Outline each uninfected red blood cell.
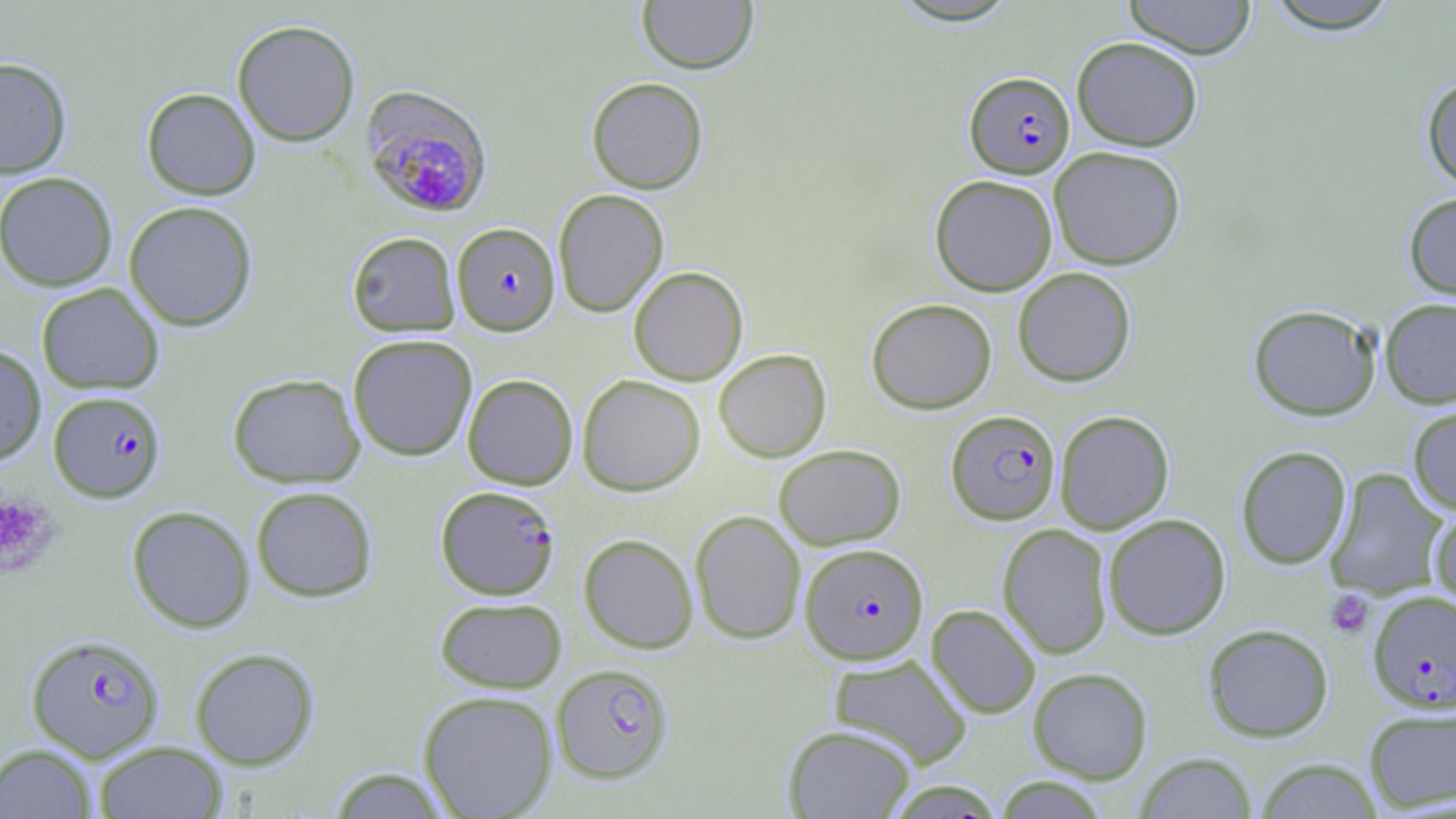

Approximate bounding boxes as [x1, y1, x2, y2] in pixels.
Uninfected red blood cells: [637, 0, 758, 75], [886, 0, 1023, 27], [1123, 0, 1258, 59], [1262, 0, 1403, 33], [232, 19, 360, 147], [1072, 36, 1203, 151], [0, 57, 72, 177], [1421, 75, 1456, 192], [586, 76, 708, 194], [141, 87, 261, 200], [1049, 146, 1186, 270], [0, 171, 117, 291], [929, 174, 1058, 296], [553, 189, 669, 317], [1403, 192, 1456, 302], [123, 200, 258, 331], [346, 231, 460, 337], [629, 266, 748, 385], [1012, 267, 1136, 387], [36, 283, 164, 394], [1380, 297, 1456, 408], [867, 298, 997, 414], [1248, 304, 1382, 421], [347, 333, 477, 461], [0, 343, 46, 465], [714, 349, 831, 462], [228, 373, 365, 488], [462, 373, 578, 489], [577, 375, 705, 496], [1408, 404, 1456, 515], [1055, 410, 1174, 534], [773, 444, 906, 549], [1236, 445, 1352, 569], [1325, 468, 1449, 600], [250, 485, 378, 602], [126, 505, 255, 633], [1428, 505, 1456, 611], [690, 510, 806, 645], [1103, 513, 1230, 640], [997, 523, 1113, 659], [578, 533, 698, 654], [434, 596, 567, 693], [927, 604, 1041, 719], [1202, 623, 1334, 742], [189, 647, 320, 770], [828, 653, 973, 769], [1028, 667, 1153, 784], [418, 690, 558, 818], [1363, 705, 1456, 813], [783, 724, 916, 819], [93, 741, 228, 819], [1, 743, 99, 819], [1135, 752, 1257, 818], [1256, 757, 1382, 818], [326, 766, 452, 818], [994, 776, 1110, 818].

Summary:
  - Plasmodium falciparum-infected red blood cell locations: [964, 71, 1075, 178], [361, 85, 493, 218], [452, 223, 560, 336], [48, 390, 166, 502], [946, 409, 1061, 525], [436, 485, 560, 600], [800, 543, 928, 665], [1368, 590, 1456, 712], [26, 633, 165, 762], [551, 663, 674, 783]
  - Platelet locations: [0, 493, 59, 580], [1325, 589, 1374, 638]
  - Slide-level diagnosis: Plasmodium falciparum
  - Field of view: single
  - Stain: May-Grünwald-Giemsa
  - Preparation: thin blood smear
  - Magnification: 1000x
  - Image size: 1456×819 pixels
  - Modality: light microscopy